Describe the morphology of the erythrocytes.
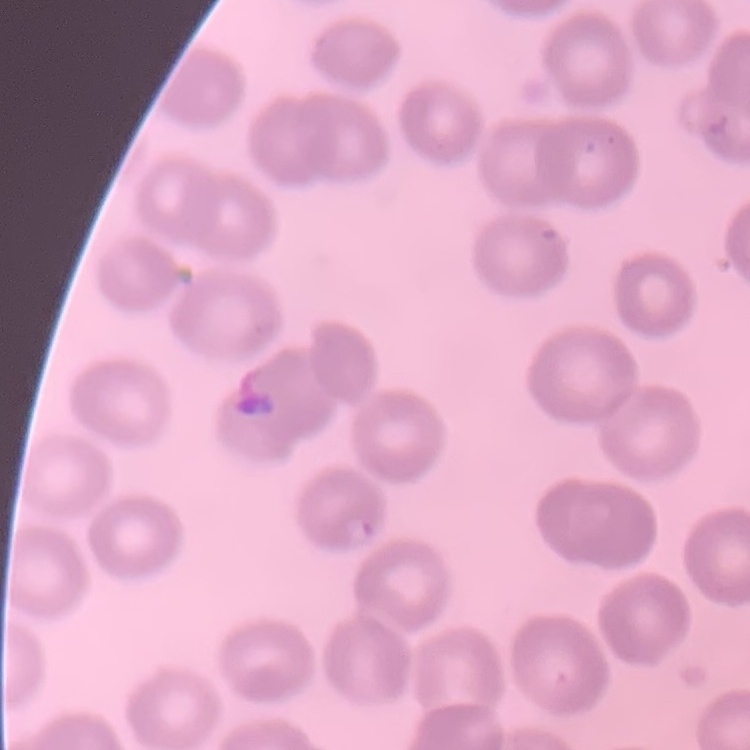

No rouleaux formation.

Summary:
  - Stain: Field's or Giemsa
  - Image type: one tile cut from a larger photomicrograph
  - Preparation: thin peripheral smear